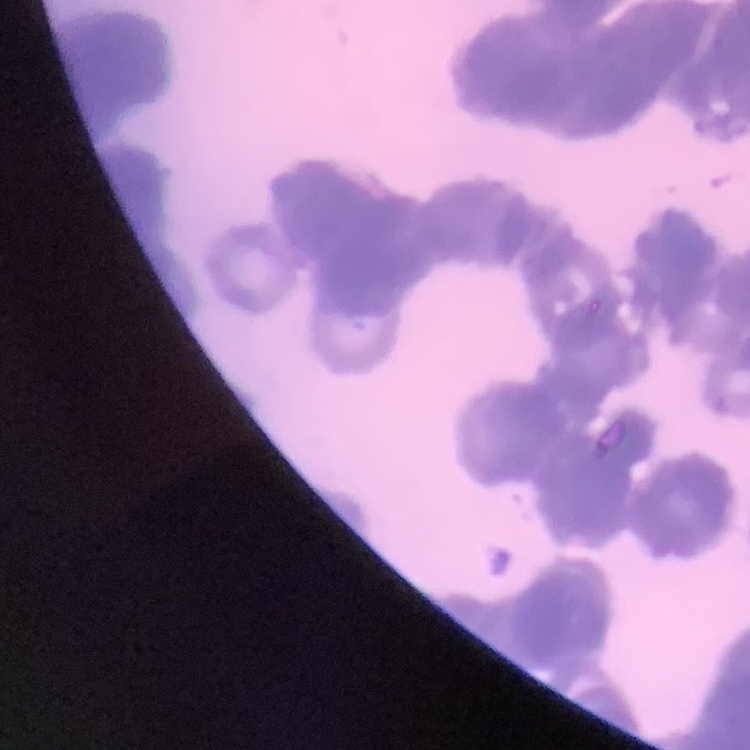
The red blood cells exhibit rouleaux formation. Stained with either Field's or Giemsa. One tile cut from a larger photomicrograph. Thin blood smear.